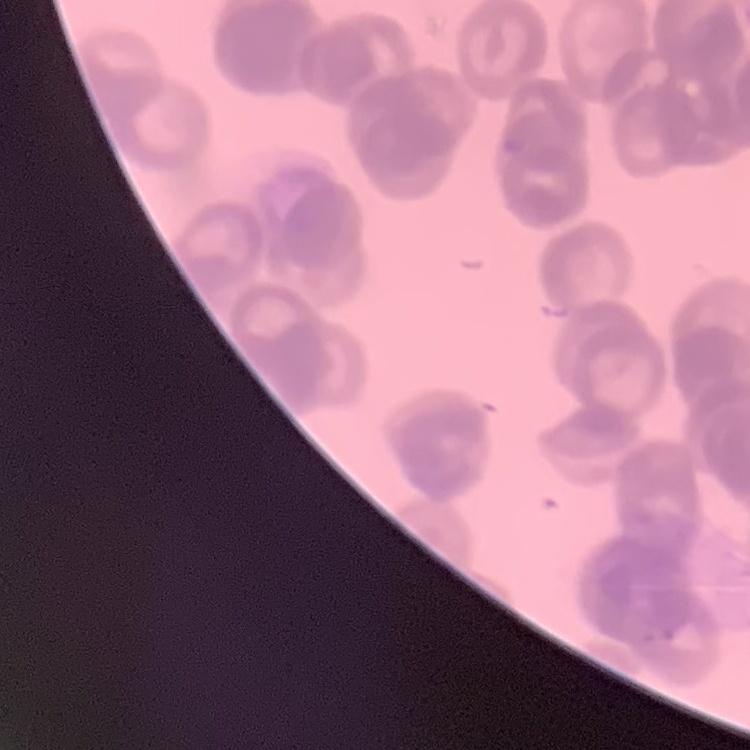

Summary:
  - Erythrocyte morphology: rouleaux formation
  - Stain: Field's or Giemsa
  - Preparation: thin peripheral smear
  - Image type: one tile cut from a larger photomicrograph